Report the malaria status of this cell.
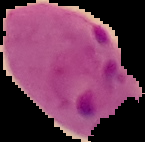
It is parasitized.

Summary:
  - Image type: segmented cell region on a black background
  - Preparation: thin blood smear
  - Image size: 145×142 pixels